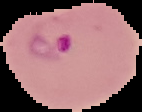

image size = 142×112 pixels
result = Plasmodium parasites detected
preparation = thin blood film
image type = segmented cell region on a black background